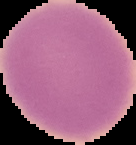
Summary:
  - Image type: segmented cell region with the area outside set to black
  - Preparation: thin blood smear
  - Image size: 136×145 pixels
  - Result: no Plasmodium parasites detected